Classify this cell by malaria status.
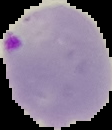

It is parasitized.

image size = 112×130 pixels
image type = segmented cell region with the area outside set to black
preparation = thin blood film